Outline each blood parasite and name the species.
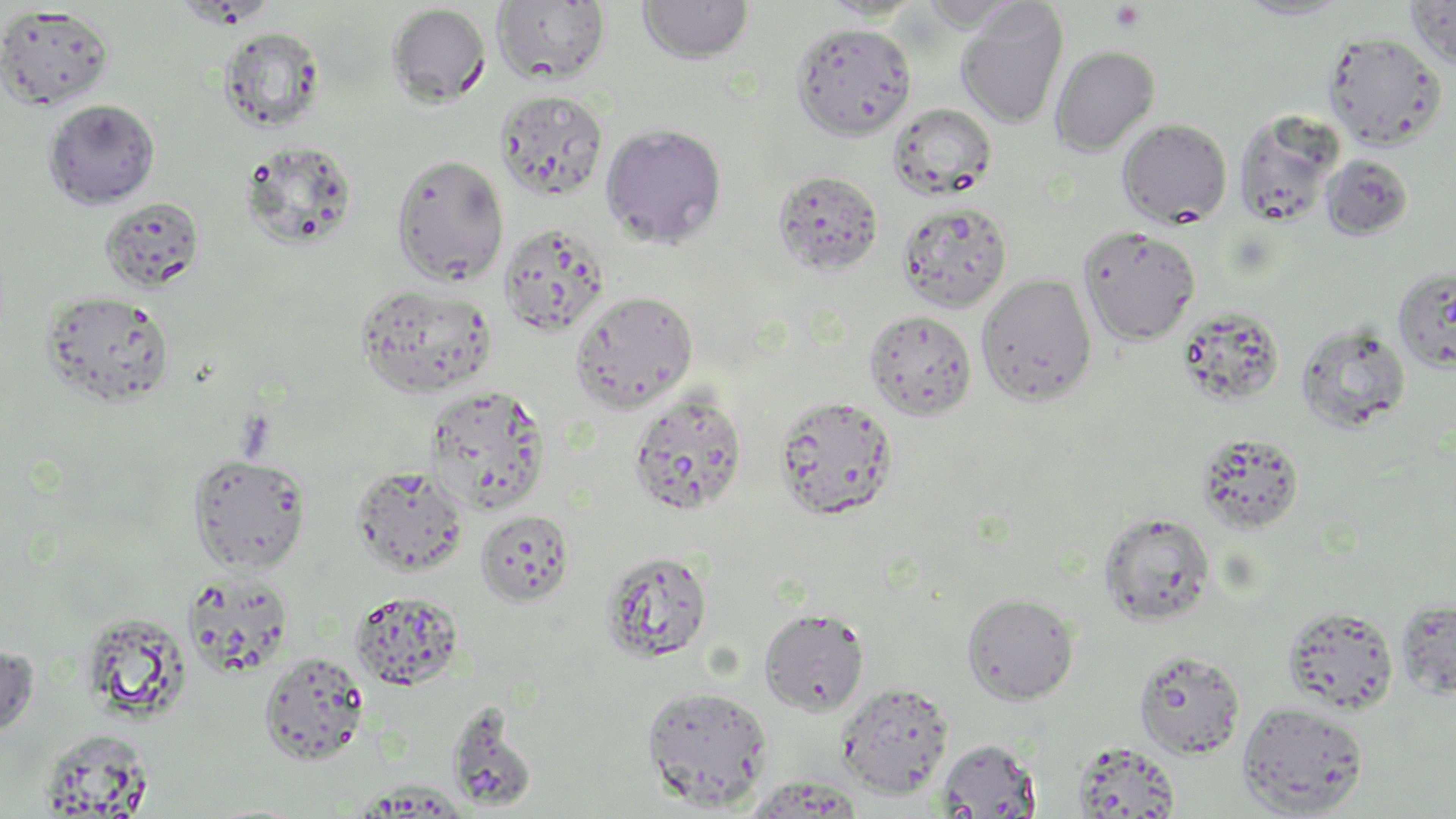
No blood parasites observed.

slide-level diagnosis = negative for blood parasites
uninfected red blood cell locations = approximate bounding boxes as [x1, y1, x2, y2] in pixels: [637, 0, 755, 63], [819, 0, 925, 21], [1233, 0, 1353, 20], [1405, 0, 1456, 69], [918, 1, 1023, 30], [955, 1, 1069, 128], [493, 2, 611, 85], [386, 3, 491, 107], [0, 5, 115, 110], [792, 22, 918, 140], [218, 26, 327, 133], [1323, 31, 1446, 151], [1049, 45, 1160, 156], [495, 90, 608, 201], [43, 99, 160, 208], [888, 102, 997, 199], [1233, 110, 1344, 228], [1117, 118, 1232, 228], [600, 123, 727, 249], [240, 141, 358, 250], [390, 152, 509, 285], [1321, 153, 1414, 240], [773, 169, 884, 276], [100, 197, 205, 292], [897, 200, 1013, 313], [498, 221, 611, 337], [1078, 224, 1201, 346], [1393, 266, 1456, 372], [976, 273, 1097, 406], [355, 282, 497, 398], [41, 290, 176, 410], [569, 291, 699, 413], [1177, 307, 1285, 407], [863, 309, 977, 420], [1297, 323, 1411, 432], [424, 385, 551, 514], [627, 390, 749, 518], [773, 394, 899, 521], [1194, 432, 1305, 535], [188, 453, 311, 573], [352, 466, 470, 577], [475, 510, 575, 606], [1098, 511, 1216, 627], [601, 549, 713, 663], [183, 573, 295, 676], [350, 590, 464, 690], [962, 592, 1079, 704], [1396, 599, 1456, 699], [1282, 605, 1399, 715], [759, 607, 870, 717], [79, 612, 192, 722], [0, 643, 38, 738], [1133, 649, 1246, 759], [259, 651, 370, 765], [836, 682, 954, 798], [641, 685, 773, 809], [448, 698, 536, 810], [1237, 699, 1370, 817], [37, 730, 155, 816], [937, 739, 1041, 818], [1071, 741, 1182, 818]
modality = optical microscopy
magnification = 1000x
platelet locations = approximate bounding boxes as [x1, y1, x2, y2] in pixels: [1109, 2, 1147, 33]
stain = May-Grünwald-Giemsa
image size = 1456×819 pixels
field of view = single
preparation = thin blood smear